Identify the blood parasite species.
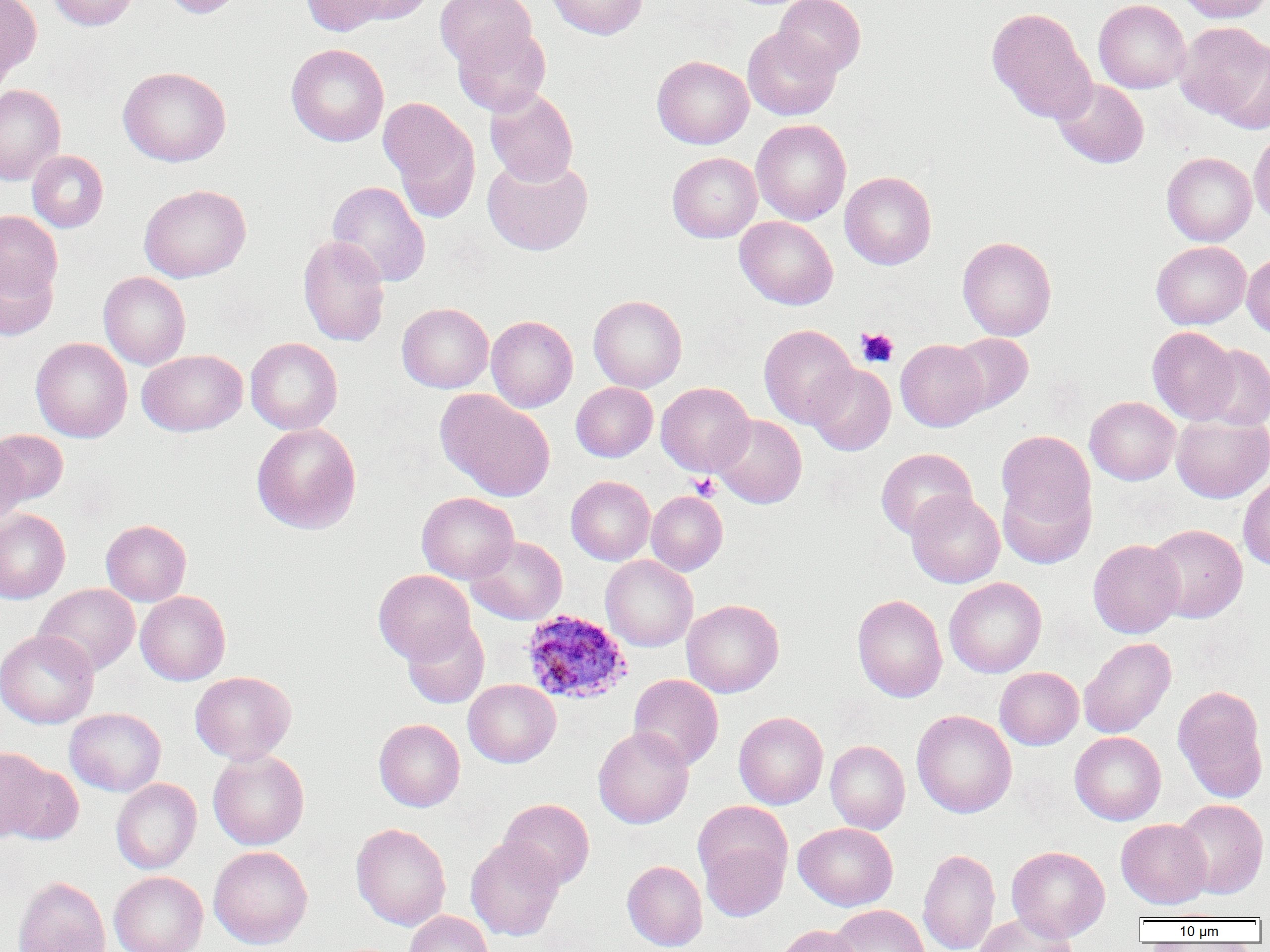

Plasmodium ovale.

Summary:
  - Coordinate format: approximate bounding boxes as named x1/y1/x2/y2 corners in pixels
  - Platelet locations: (x1=856, y1=327, x2=899, y2=368), (x1=688, y1=473, x2=721, y2=500)
  - Plasmodium ovale-infected red blood cell locations: (x1=521, y1=609, x2=631, y2=705)
  - Uninfected red blood cell locations: (x1=0, y1=0, x2=41, y2=80), (x1=46, y1=0, x2=138, y2=30), (x1=160, y1=0, x2=245, y2=18), (x1=301, y1=0, x2=388, y2=36), (x1=346, y1=0, x2=436, y2=24), (x1=435, y1=0, x2=536, y2=68), (x1=546, y1=0, x2=647, y2=39), (x1=773, y1=0, x2=866, y2=77), (x1=1093, y1=0, x2=1191, y2=93), (x1=1176, y1=0, x2=1270, y2=23), (x1=986, y1=7, x2=1096, y2=124), (x1=1176, y1=22, x2=1270, y2=125), (x1=453, y1=26, x2=551, y2=117), (x1=743, y1=27, x2=841, y2=121), (x1=286, y1=43, x2=389, y2=146), (x1=652, y1=56, x2=753, y2=149), (x1=118, y1=66, x2=231, y2=167), (x1=1052, y1=78, x2=1149, y2=168), (x1=0, y1=84, x2=65, y2=185), (x1=485, y1=88, x2=578, y2=186), (x1=379, y1=97, x2=481, y2=220), (x1=751, y1=119, x2=851, y2=225), (x1=1249, y1=128, x2=1270, y2=228), (x1=27, y1=150, x2=108, y2=232), (x1=667, y1=152, x2=762, y2=242), (x1=1162, y1=152, x2=1257, y2=246), (x1=483, y1=155, x2=593, y2=256), (x1=840, y1=171, x2=937, y2=270), (x1=327, y1=181, x2=431, y2=287), (x1=139, y1=184, x2=251, y2=283), (x1=0, y1=211, x2=63, y2=302), (x1=735, y1=216, x2=838, y2=309), (x1=297, y1=235, x2=390, y2=347), (x1=957, y1=236, x2=1057, y2=340), (x1=1151, y1=241, x2=1251, y2=330), (x1=1242, y1=252, x2=1270, y2=339), (x1=0, y1=257, x2=58, y2=341), (x1=98, y1=271, x2=191, y2=370), (x1=588, y1=295, x2=687, y2=392), (x1=397, y1=303, x2=493, y2=393), (x1=486, y1=315, x2=578, y2=412), (x1=759, y1=324, x2=858, y2=428), (x1=1147, y1=326, x2=1239, y2=424), (x1=947, y1=333, x2=1033, y2=416), (x1=30, y1=337, x2=132, y2=442), (x1=245, y1=337, x2=343, y2=435), (x1=896, y1=339, x2=989, y2=431), (x1=1197, y1=344, x2=1270, y2=430), (x1=137, y1=349, x2=248, y2=436), (x1=806, y1=363, x2=896, y2=456), (x1=656, y1=381, x2=754, y2=477), (x1=571, y1=382, x2=657, y2=462), (x1=435, y1=389, x2=555, y2=502), (x1=1085, y1=396, x2=1181, y2=485), (x1=1171, y1=414, x2=1270, y2=503), (x1=712, y1=415, x2=807, y2=508), (x1=251, y1=422, x2=362, y2=534), (x1=996, y1=428, x2=1096, y2=540), (x1=1, y1=429, x2=68, y2=506), (x1=0, y1=436, x2=29, y2=528), (x1=876, y1=448, x2=977, y2=540), (x1=566, y1=475, x2=655, y2=565), (x1=997, y1=475, x2=1095, y2=569), (x1=1238, y1=475, x2=1270, y2=571), (x1=906, y1=490, x2=1005, y2=588), (x1=646, y1=491, x2=728, y2=575), (x1=416, y1=492, x2=519, y2=584), (x1=0, y1=509, x2=70, y2=603), (x1=101, y1=519, x2=191, y2=606), (x1=1147, y1=523, x2=1248, y2=622), (x1=466, y1=535, x2=567, y2=624), (x1=1088, y1=539, x2=1185, y2=638), (x1=600, y1=555, x2=698, y2=651), (x1=374, y1=569, x2=475, y2=664), (x1=944, y1=577, x2=1047, y2=678), (x1=35, y1=583, x2=140, y2=675), (x1=135, y1=591, x2=231, y2=685), (x1=852, y1=594, x2=948, y2=702), (x1=681, y1=599, x2=784, y2=697), (x1=402, y1=618, x2=489, y2=708), (x1=0, y1=629, x2=99, y2=728), (x1=1078, y1=637, x2=1176, y2=738), (x1=995, y1=667, x2=1084, y2=750), (x1=190, y1=671, x2=296, y2=764), (x1=629, y1=674, x2=724, y2=771), (x1=463, y1=679, x2=561, y2=767), (x1=1172, y1=685, x2=1269, y2=802), (x1=64, y1=707, x2=166, y2=796), (x1=911, y1=709, x2=1017, y2=818), (x1=734, y1=711, x2=828, y2=809), (x1=374, y1=718, x2=465, y2=811), (x1=593, y1=726, x2=693, y2=829), (x1=1069, y1=732, x2=1166, y2=825), (x1=825, y1=740, x2=910, y2=834), (x1=207, y1=749, x2=309, y2=850), (x1=1, y1=758, x2=84, y2=845), (x1=111, y1=778, x2=201, y2=873), (x1=498, y1=798, x2=594, y2=890), (x1=1173, y1=799, x2=1269, y2=899), (x1=692, y1=801, x2=792, y2=892), (x1=1116, y1=819, x2=1212, y2=908), (x1=793, y1=822, x2=898, y2=911), (x1=351, y1=823, x2=451, y2=931), (x1=698, y1=835, x2=790, y2=922), (x1=465, y1=837, x2=565, y2=941), (x1=209, y1=845, x2=313, y2=949), (x1=1006, y1=846, x2=1110, y2=941), (x1=917, y1=848, x2=1000, y2=952), (x1=622, y1=860, x2=707, y2=951), (x1=109, y1=871, x2=208, y2=952), (x1=12, y1=875, x2=110, y2=952), (x1=828, y1=904, x2=929, y2=952), (x1=404, y1=911, x2=494, y2=952), (x1=974, y1=913, x2=1076, y2=952), (x1=773, y1=925, x2=864, y2=952)
  - Modality: light microscopy
  - Preparation: thin blood smear
  - Field of view: one of a larger specimen
  - Magnification: 1000x
  - Image size: 1270×952 pixels